Classify this cell by malaria status.
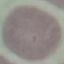

Uninfected.

Photographed with a smartphone camera at the microscope eyepiece. Cell patch, automatically extracted from a larger field of view and resized to 64 × 64 pixels. Thin blood smear. Giemsa-stained preparation.